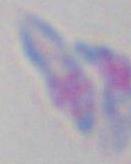
modality = photomicrograph
identification = Toxoplasma gondii
magnification = 1000x